State which parasite is depicted.
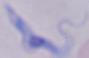

This is a trypanosome.

Captured at 1000x magnification. Micrograph.